Assess this cell for malaria.
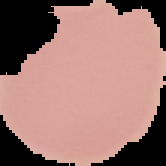
Uninfected.

Image is 166×166 pixels. The area outside the segmented cell region is set to black. From a thin blood film.